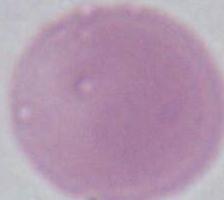

Summary:
  - Modality: micrograph
  - Magnification: 1000x
  - Identification: erythrocyte